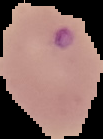
{
  "image_type": "segmented cell region on a black background",
  "result": "Plasmodium parasites detected",
  "image_size": "103×139 pixels",
  "preparation": "thin blood smear"
}